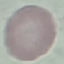

{
  "result": "no malaria parasites detected",
  "capture": "smartphone through the microscope eyepiece",
  "stain": "Giemsa",
  "preparation": "thin blood smear",
  "image_type": "cell patch, automatically extracted from a larger field of view and resized to 64 × 64 pixels"
}